State which cell type is depicted.
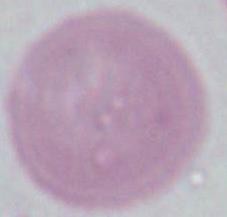
This is an erythrocyte.

Summary:
  - Modality: micrograph
  - Magnification: 1000x